Identify the parasite.
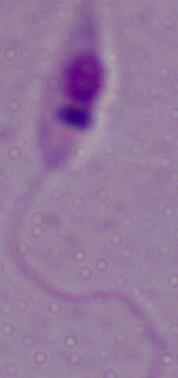

Leishmania.

Micrograph. Captured at 1000x magnification.